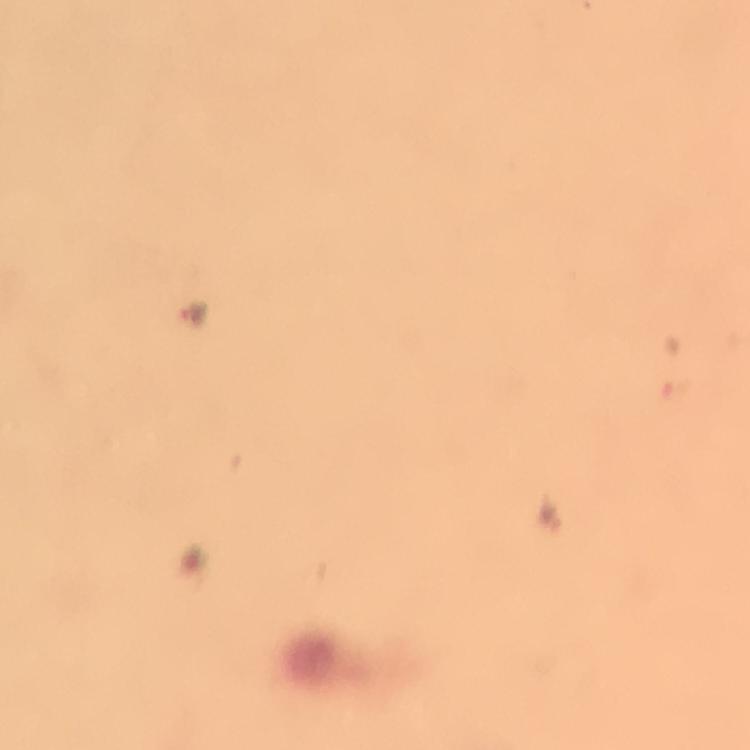

Approximate centers as {x, y} in pixels.
Summary:
  - Malaria parasite locations: {197, 312}, {553, 514}
  - Context: from a diagnostic examination for malaria
  - Stain: Giemsa
  - Preparation: thick smear
  - Capture: smartphone camera through the microscope
  - Cropped from: one field of view
  - Magnification: 100x
  - Immersion oil: applied
  - Image size: 750×750 pixels